Assess this cell for malaria.
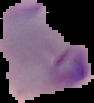
Parasitized.

preparation = thin blood film
image size = 94×103 pixels
image type = segmented cell region on a black background